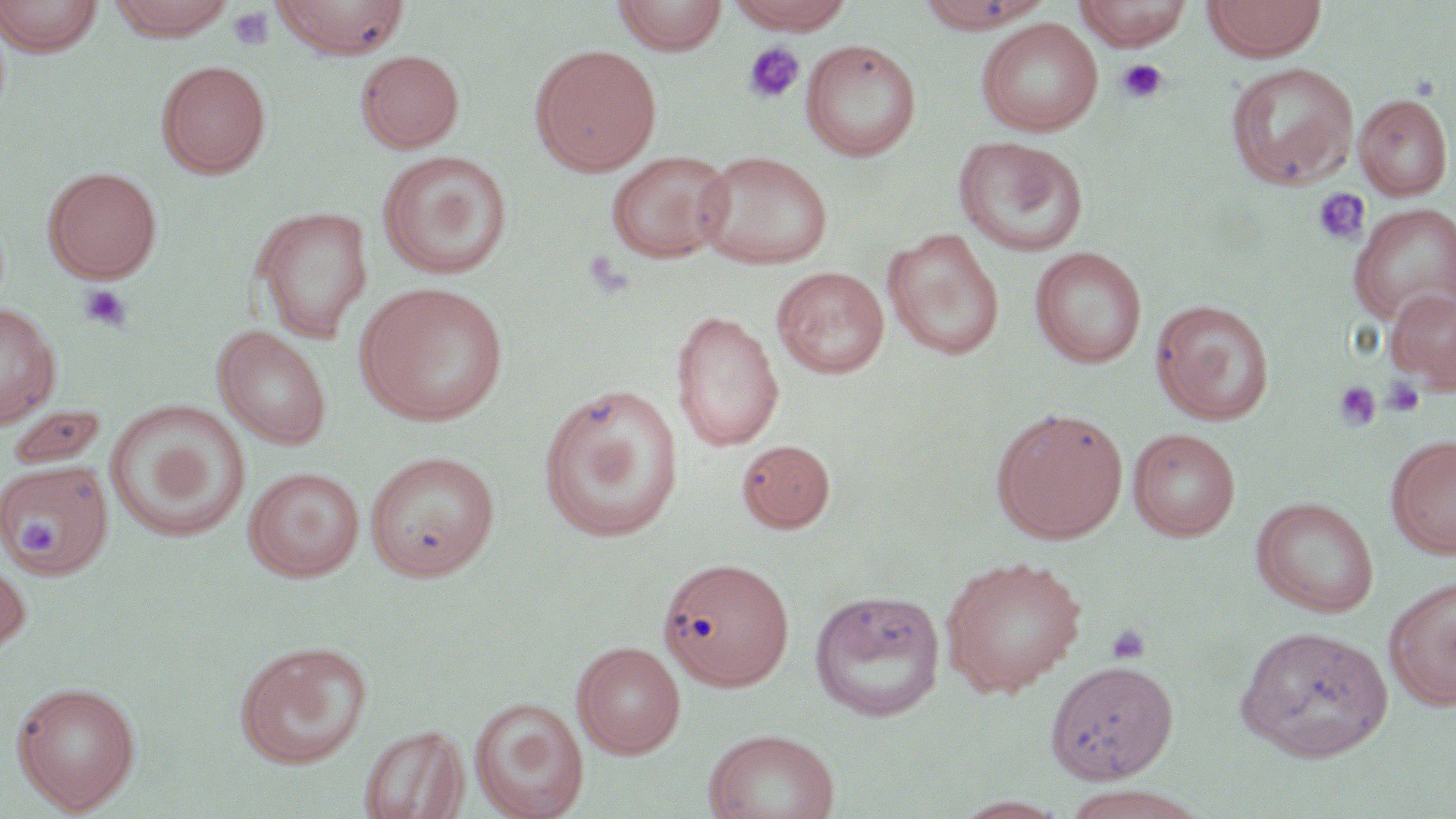
slide_level_diagnosis: negative for blood parasites
field_of_view: one of a larger specimen
uninfected_red_blood_cell_locations: 'approximate bounding boxes as named x1/y1/x2/y2 corners in pixels: (x1=0, y1=0, x2=104, y2=58), (x1=106, y1=0, x2=236, y2=41), (x1=272, y1=0, x2=412, y2=59), (x1=612, y1=0, x2=729, y2=55), (x1=726, y1=0, x2=855, y2=34), (x1=913, y1=0, x2=1055, y2=33), (x1=1074, y1=0, x2=1194, y2=50), (x1=1201, y1=0, x2=1327, y2=61), (x1=976, y1=18, x2=1103, y2=137), (x1=800, y1=40, x2=922, y2=161), (x1=530, y1=43, x2=663, y2=176), (x1=356, y1=49, x2=465, y2=153), (x1=156, y1=60, x2=272, y2=178), (x1=1225, y1=62, x2=1358, y2=189), (x1=1354, y1=93, x2=1453, y2=201), (x1=953, y1=136, x2=1089, y2=258), (x1=377, y1=150, x2=512, y2=281), (x1=606, y1=150, x2=734, y2=264), (x1=694, y1=150, x2=834, y2=270), (x1=43, y1=165, x2=163, y2=283), (x1=1349, y1=203, x2=1456, y2=324), (x1=251, y1=206, x2=374, y2=343), (x1=881, y1=229, x2=1005, y2=361), (x1=1029, y1=246, x2=1147, y2=368), (x1=772, y1=266, x2=890, y2=379), (x1=356, y1=282, x2=509, y2=426), (x1=1385, y1=286, x2=1456, y2=392), (x1=1150, y1=298, x2=1275, y2=425), (x1=0, y1=302, x2=61, y2=430), (x1=671, y1=308, x2=784, y2=451), (x1=213, y1=325, x2=332, y2=450), (x1=538, y1=383, x2=684, y2=543), (x1=105, y1=400, x2=251, y2=544), (x1=6, y1=403, x2=109, y2=469), (x1=991, y1=407, x2=1128, y2=544), (x1=1128, y1=428, x2=1240, y2=541), (x1=1386, y1=434, x2=1456, y2=558), (x1=737, y1=439, x2=836, y2=532), (x1=365, y1=450, x2=500, y2=581), (x1=0, y1=457, x2=114, y2=579), (x1=243, y1=466, x2=366, y2=582), (x1=1250, y1=496, x2=1380, y2=617), (x1=0, y1=550, x2=31, y2=661), (x1=654, y1=555, x2=794, y2=694), (x1=939, y1=555, x2=1087, y2=696), (x1=1384, y1=576, x2=1456, y2=711), (x1=808, y1=588, x2=946, y2=722), (x1=1234, y1=625, x2=1393, y2=762), (x1=234, y1=641, x2=373, y2=768), (x1=572, y1=641, x2=686, y2=759), (x1=1046, y1=660, x2=1179, y2=783), (x1=11, y1=680, x2=142, y2=814), (x1=470, y1=696, x2=589, y2=819), (x1=358, y1=724, x2=469, y2=819), (x1=703, y1=727, x2=840, y2=819), (x1=1056, y1=786, x2=1205, y2=819), (x1=952, y1=795, x2=1070, y2=818)'
platelet_locations: 'approximate bounding boxes as named x1/y1/x2/y2 corners in pixels: (x1=228, y1=6, x2=275, y2=51), (x1=743, y1=42, x2=807, y2=105), (x1=1116, y1=58, x2=1168, y2=104), (x1=1312, y1=187, x2=1370, y2=246), (x1=78, y1=284, x2=132, y2=332), (x1=1381, y1=377, x2=1426, y2=418), (x1=1333, y1=380, x2=1382, y2=432), (x1=18, y1=506, x2=73, y2=561), (x1=1106, y1=623, x2=1151, y2=665)'
magnification: 1000x
modality: optical microscopy
stain: May-Grünwald-Giemsa
image_size: 1456×819 pixels
preparation: thin blood film